Report the malaria status of this cell.
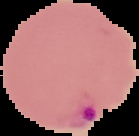
It is parasitized.

Image is 139×136 pixels. From a thin blood smear. Segmented cell region on a black background.